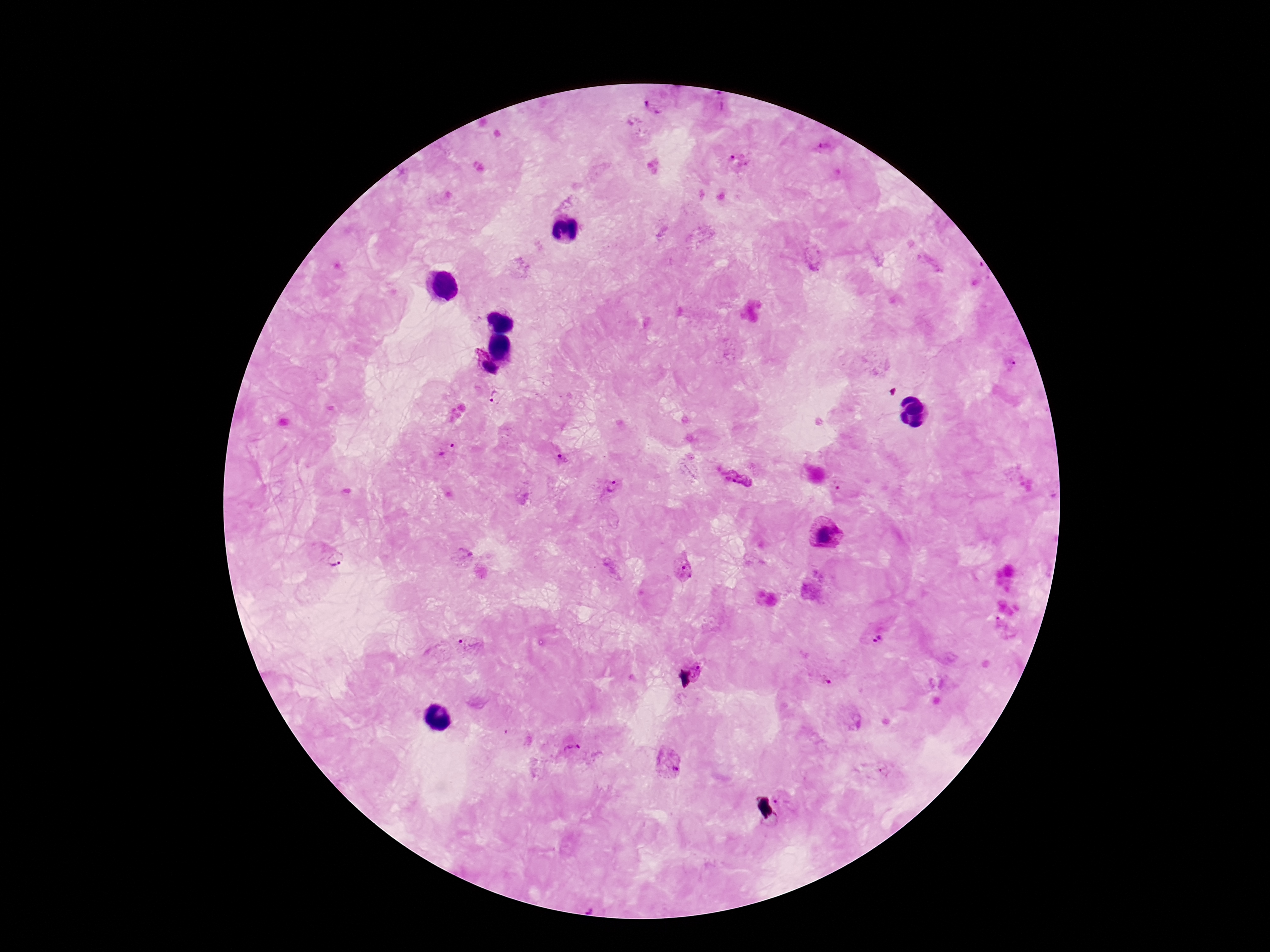
Approximate object centers, in pixels from the top-left corner.
Summary:
  - Plasmodium parasite locations: (x=720, y=104), (x=653, y=106), (x=825, y=147), (x=740, y=161), (x=983, y=273), (x=1009, y=364), (x=487, y=366), (x=496, y=397), (x=447, y=450), (x=562, y=459), (x=738, y=478), (x=838, y=484), (x=611, y=487), (x=825, y=534), (x=333, y=562), (x=684, y=570), (x=1004, y=628), (x=874, y=631), (x=462, y=648), (x=698, y=668), (x=822, y=678), (x=570, y=746), (x=667, y=761), (x=885, y=774), (x=783, y=804)
  - Capture: smartphone camera through the microscope eyepiece
  - Field of view: single
  - Patient malaria status: infected
  - Magnification: 100x
  - Preparation: thick blood smear
  - Image size: 1270×952 pixels
  - Stain: Giemsa